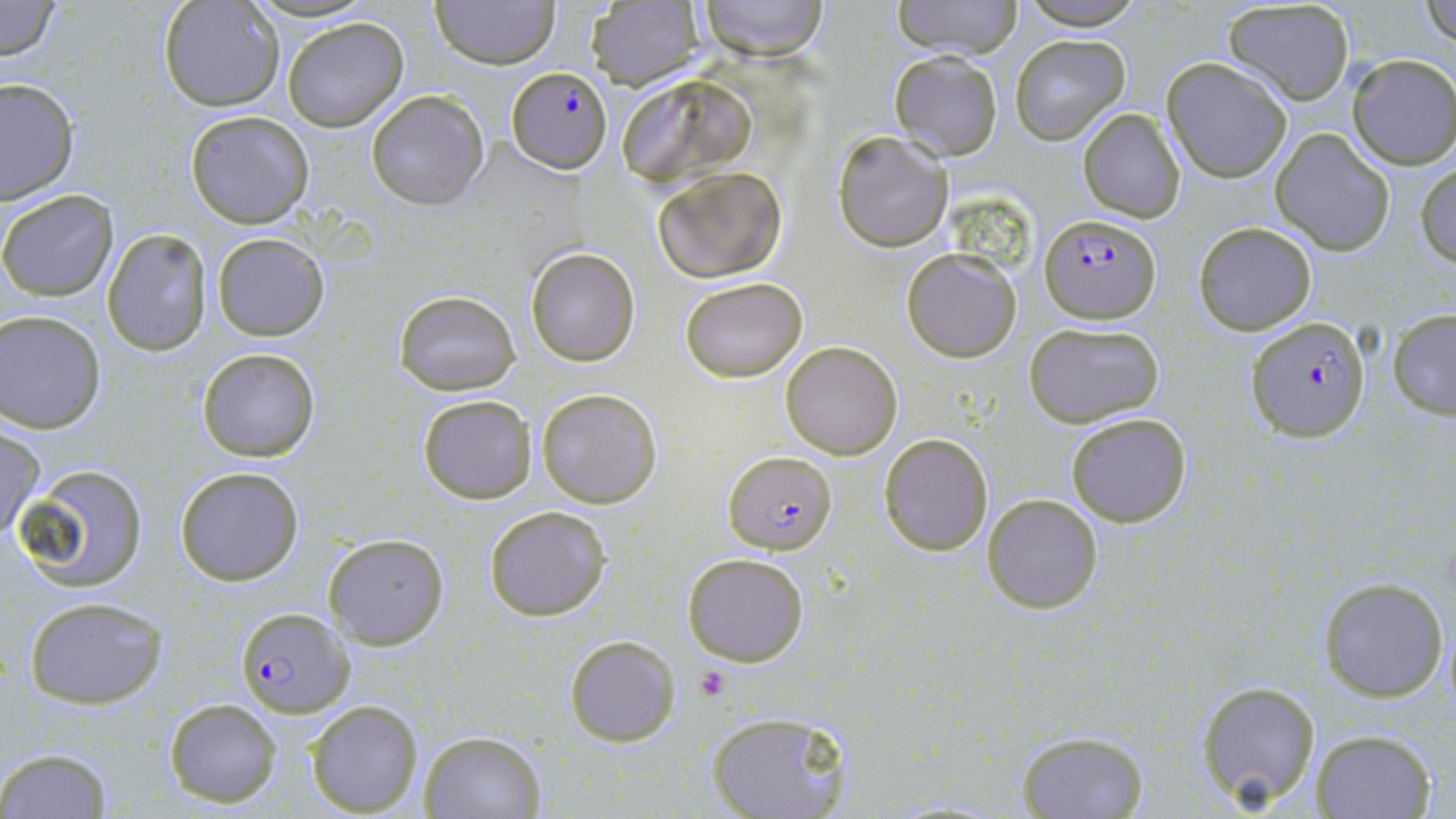
slide-level diagnosis = Plasmodium falciparum
stain = May-Grünwald-Giemsa
preparation = thin blood film
platelet locations = approximate bounding boxes as (x1, y1, x2, y2) in pixels: (696, 666, 729, 702)
field of view = one of a larger specimen
Plasmodium falciparum-infected red blood cell locations = approximate bounding boxes as (x1, y1, x2, y2) in pixels: (506, 67, 610, 173), (1038, 215, 1163, 324), (1249, 317, 1371, 441), (723, 451, 836, 553), (236, 607, 353, 717)
magnification = 1000x
uninfected red blood cell locations = approximate bounding boxes as (x1, y1, x2, y2) in pixels: (0, 0, 63, 61), (160, 0, 284, 112), (430, 0, 560, 69), (694, 0, 832, 61), (893, 0, 1023, 59), (1422, 0, 1455, 50), (1017, 1, 1150, 29), (585, 2, 705, 89), (1223, 2, 1355, 104), (283, 18, 408, 132), (1010, 34, 1130, 144), (888, 51, 1003, 162), (1346, 54, 1456, 169), (1163, 58, 1293, 182), (615, 71, 762, 186), (0, 77, 77, 206), (366, 92, 489, 209), (1077, 107, 1186, 222), (185, 110, 314, 228), (1271, 128, 1395, 256), (832, 130, 954, 252), (1416, 160, 1456, 266), (652, 166, 787, 282), (0, 190, 119, 301), (1193, 221, 1317, 334), (103, 230, 211, 354), (213, 233, 329, 340), (526, 247, 640, 366), (901, 247, 1023, 363), (680, 277, 806, 383), (393, 289, 519, 395), (1387, 310, 1456, 418), (1, 312, 106, 432), (1026, 320, 1164, 428), (781, 341, 902, 459), (196, 347, 321, 462), (536, 387, 663, 508), (418, 394, 537, 504), (1066, 412, 1192, 527), (1, 428, 44, 540), (878, 433, 993, 556), (20, 465, 148, 590), (174, 466, 304, 586), (982, 493, 1104, 614), (484, 504, 612, 622), (323, 533, 450, 649), (683, 552, 810, 667), (1319, 576, 1449, 701), (22, 597, 167, 707), (566, 636, 678, 746), (1196, 680, 1322, 809), (162, 698, 283, 808), (307, 700, 423, 817), (707, 712, 850, 819), (418, 729, 546, 818), (1014, 729, 1149, 818), (1311, 730, 1436, 818), (1, 748, 116, 819)
modality = optical microscopy
image size = 1456×819 pixels